Identify the cell.
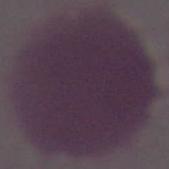

This is an erythrocyte.

modality = micrograph
magnification = 1000x